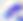 Toxoplasma gondii is shown. Captured at 400x magnification. Micrograph.